Assess this cell for malaria.
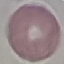
Uninfected.

{
  "image_type": "cell patch, automatically extracted from a larger field of view and resized to 64 × 64 pixels",
  "capture": "smartphone through the microscope eyepiece",
  "preparation": "thin blood smear",
  "stain": "Giemsa"
}